Outline platelets.
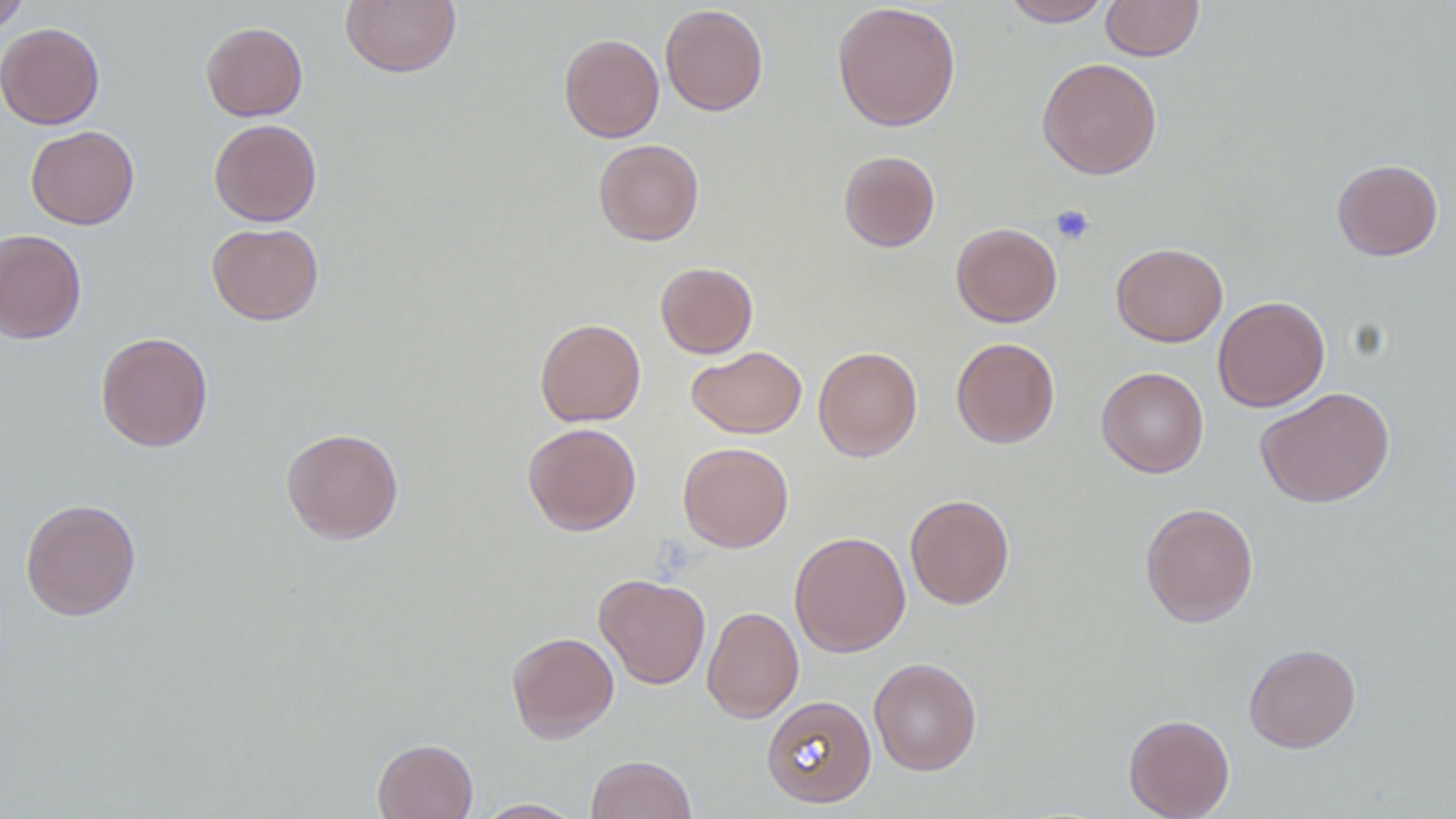

Approximate bounding boxes as (x1,y1)-(x2,y2) corner pairs in pixels.
Platelets: (1050,204)-(1096,246).

Summary:
  - Uninfected red blood cell locations: (0,0)-(32,34), (340,0)-(461,78), (1001,0)-(1112,27), (1101,0)-(1203,61), (831,2)-(961,132), (660,4)-(768,116), (201,21)-(308,121), (0,23)-(105,130), (559,33)-(664,143), (1037,57)-(1163,179), (209,118)-(322,226), (25,125)-(139,229), (593,139)-(704,245), (838,150)-(940,252), (1332,158)-(1443,261), (207,222)-(324,325), (951,222)-(1062,327), (0,228)-(86,344), (1111,242)-(1228,347), (655,262)-(758,358), (1213,296)-(1330,412), (535,318)-(646,426), (95,331)-(213,452), (951,337)-(1060,448), (813,345)-(922,461), (687,346)-(807,438), (1096,366)-(1209,478), (1255,387)-(1395,508), (523,422)-(641,535), (280,427)-(403,544), (678,441)-(793,552), (905,494)-(1015,609), (20,498)-(141,620), (1140,502)-(1259,627), (788,531)-(911,657), (594,573)-(711,689), (702,606)-(803,722), (506,631)-(619,743), (1244,643)-(1361,752), (868,657)-(982,776), (761,696)-(877,808), (1123,714)-(1235,819), (372,738)-(477,819), (586,754)-(697,819), (473,799)-(585,818)
  - Slide-level diagnosis: no evidence of blood parasites
  - Field of view: single
  - Magnification: 1000x
  - Preparation: thin blood film
  - Image size: 1456×819 pixels
  - Modality: light microscopy